Assess the morphology of the erythrocytes.
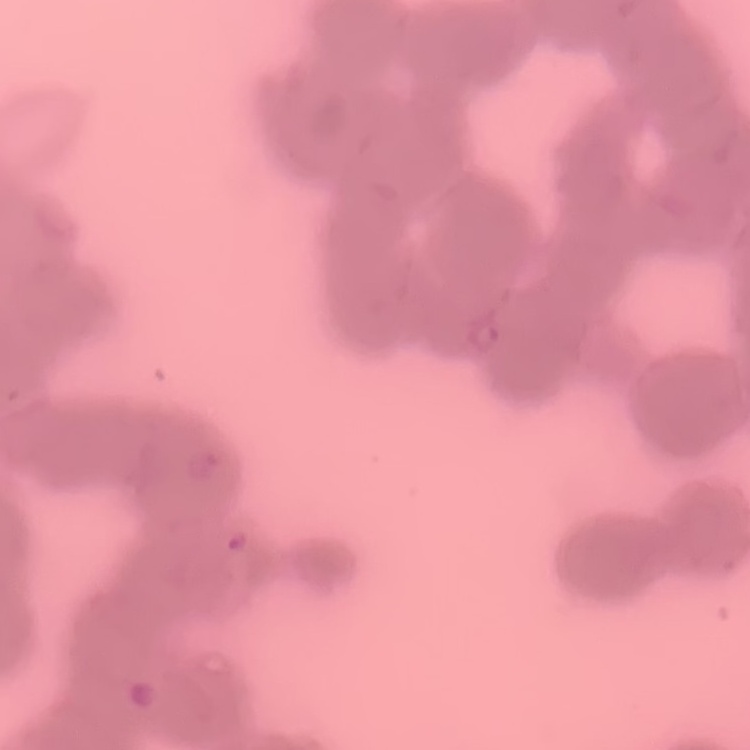

Rouleaux formation.

image_type: one tile cut from a larger photomicrograph
stain: Field's or Giemsa
preparation: thin blood smear